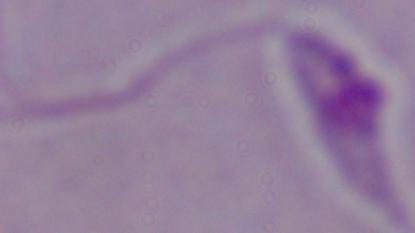
Captured at 1000x magnification. A Leishmania parasite is shown. Photomicrograph.